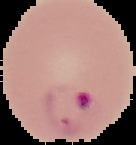
preparation = thin blood smear
image type = segmented cell region with the area outside set to black
malaria status = parasitized
image size = 136×145 pixels